Identify the cell.
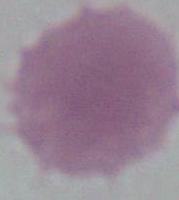
An erythrocyte.

Summary:
  - Modality: micrograph
  - Magnification: 1000x